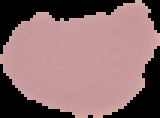
Summary:
  - Image type: segmented cell region on a black background
  - Preparation: thin blood smear
  - Result: no malaria parasites detected
  - Image size: 160×118 pixels